Name the parasite shown.
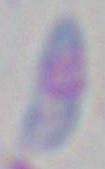

Toxoplasma gondii.

Summary:
  - Magnification: 1000x
  - Modality: micrograph